Give the position of every malaria parasite.
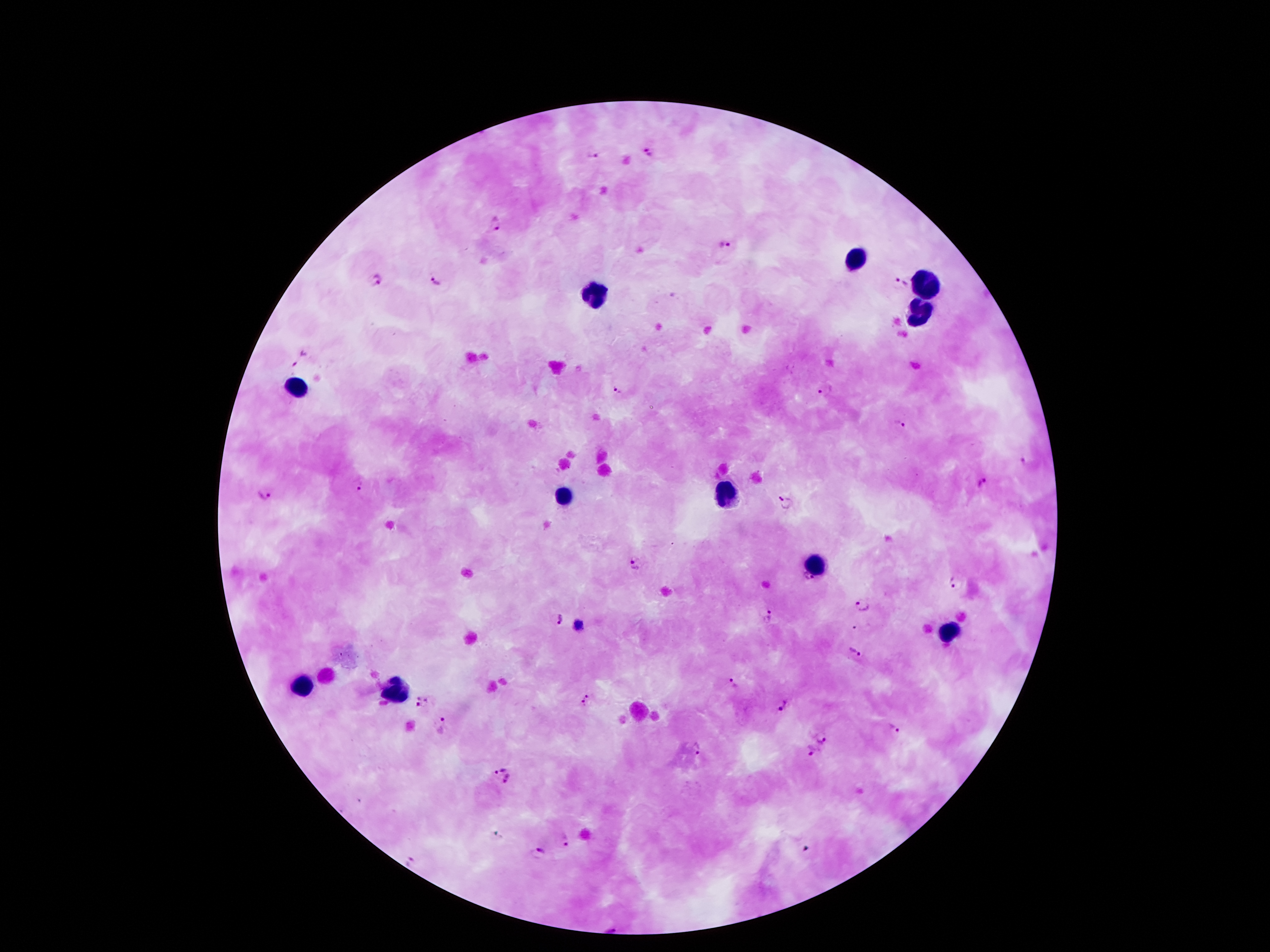

Approximate object centers, in pixels from the top-left corner.
Malaria parasites: (x=595, y=153), (x=647, y=154), (x=495, y=223), (x=725, y=246), (x=376, y=280), (x=435, y=281), (x=901, y=283), (x=300, y=359), (x=827, y=389), (x=619, y=391), (x=898, y=424), (x=1023, y=461), (x=984, y=483), (x=358, y=485), (x=263, y=495), (x=786, y=503), (x=636, y=564), (x=955, y=583), (x=863, y=607), (x=770, y=615), (x=559, y=621), (x=854, y=654), (x=732, y=684), (x=587, y=701), (x=422, y=702), (x=782, y=706), (x=448, y=722), (x=895, y=729), (x=822, y=735), (x=695, y=749), (x=810, y=749), (x=501, y=766), (x=508, y=779), (x=566, y=839), (x=541, y=854), (x=412, y=862), (x=611, y=929).

leukocyte locations = (x=855, y=259), (x=929, y=286), (x=598, y=291), (x=919, y=310), (x=297, y=382), (x=724, y=493), (x=561, y=498), (x=813, y=565), (x=949, y=632), (x=299, y=686), (x=393, y=686)
image size = 1270×952 pixels
patient malaria status = infected with Plasmodium falciparum
magnification = 100x
stain = Giemsa
field of view = one from this slide
preparation = thick peripheral-blood smear
capture = smartphone through the microscope eyepiece